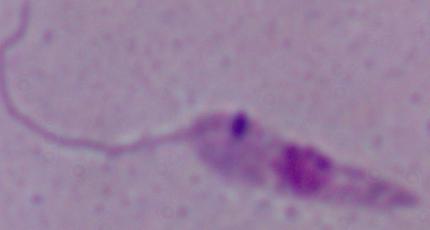
Captured at 1000x magnification. A Leishmania parasite is shown. Photomicrograph.